Draw a bounding box around every leukocyte (white blood cell).
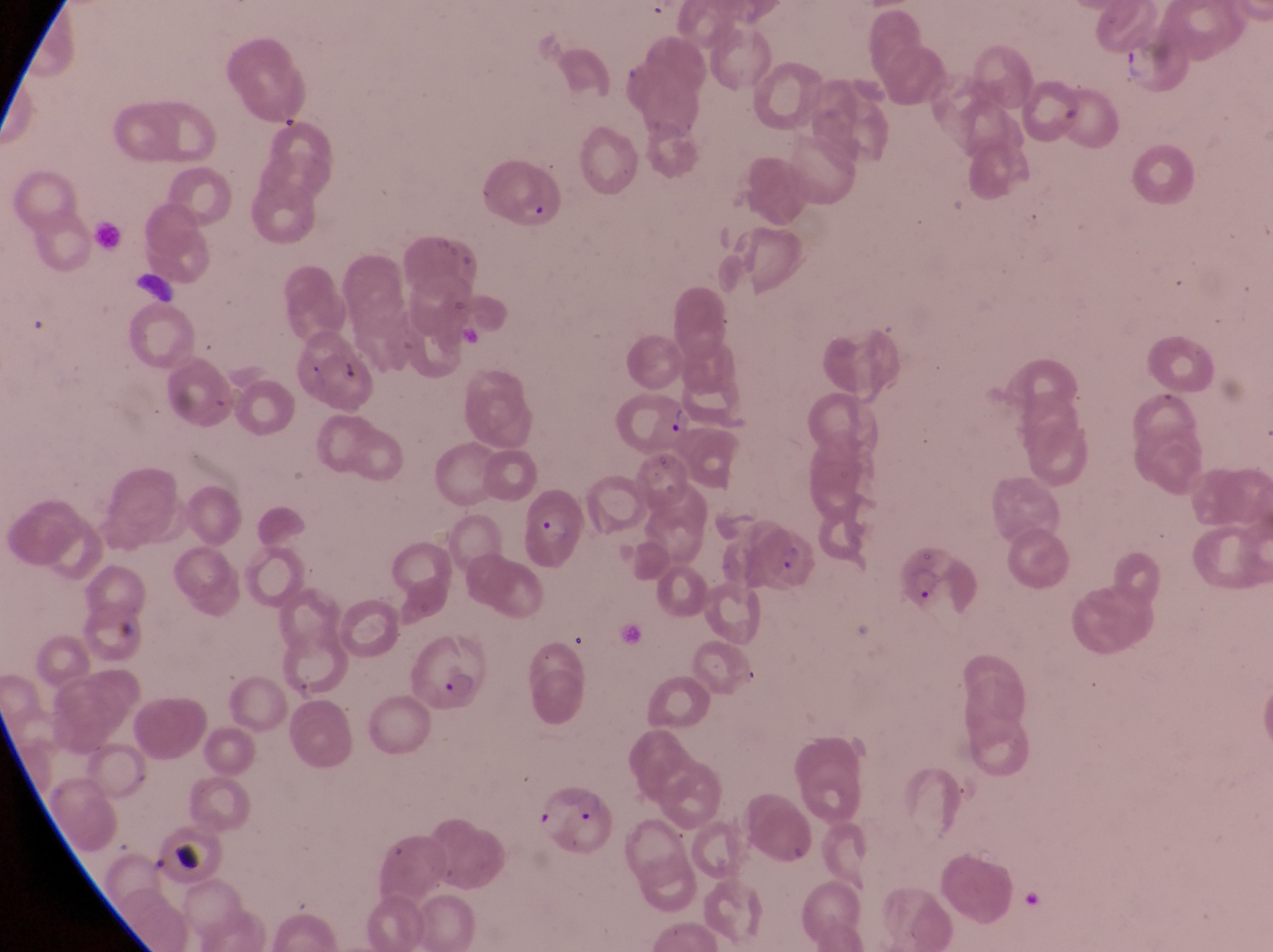
No leukocytes observed.

image size = 1273×952 pixels
capture = smartphone photograph through the eyepiece of an Olympus CX-23 microscope
country = Uganda
gametocyte locations = approximate bounding boxes as {left, top, right, bottom} in pixels: {127, 267, 182, 309}
artifact (platelet-like body, stain precipitate, or debris) locations = approximate bounding boxes as {left, top, right, bottom} in pixels: {664, 404, 696, 443}, {169, 842, 199, 874}
parasitised red blood cell locations = approximate bounding boxes as {left, top, right, bottom} in pixels: {475, 167, 563, 235}, {519, 494, 584, 569}, {762, 530, 825, 600}, {899, 542, 981, 634}, {404, 634, 489, 708}, {522, 779, 612, 862}
magnification = 1000x
field of view = single
preparation = thin blood smear